Locate every blood parasite and identify its species.
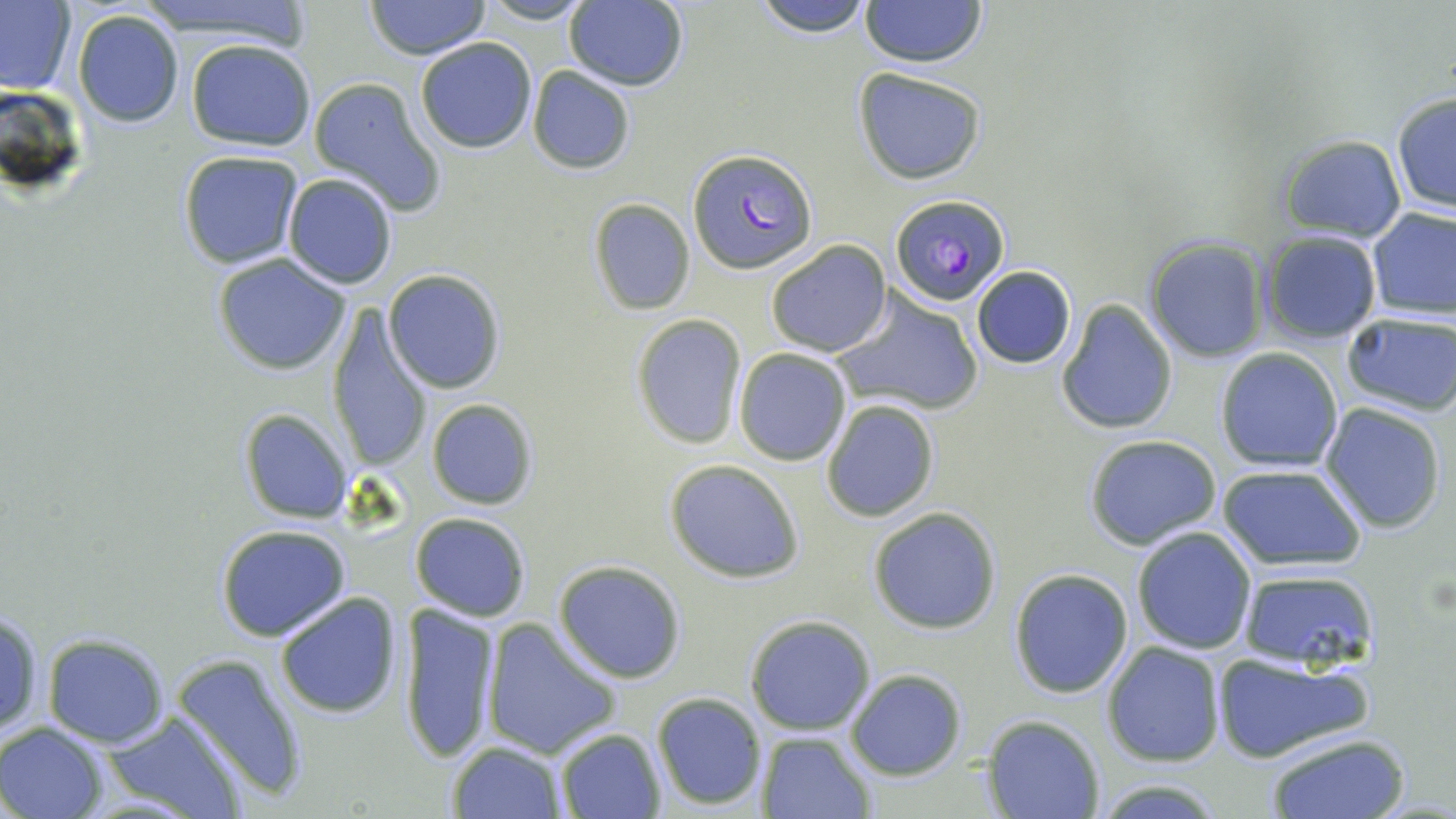
Approximate bounding boxes as (x1, y1, x2, y2) in pixels.
Plasmodium falciparum-infected red blood cells: (688, 148, 814, 274), (890, 194, 1011, 305).
No Plasmodium ovale, Plasmodium malariae, Plasmodium vivax, Babesia divergens, or Trypanosoma brucei observed.

Summary:
  - Uninfected red blood cell locations: (0, 0, 77, 98), (133, 0, 318, 41), (364, 0, 492, 61), (476, 0, 596, 25), (752, 0, 873, 38), (857, 0, 988, 69), (563, 1, 689, 91), (72, 7, 186, 129), (414, 38, 537, 154), (184, 39, 317, 153), (527, 66, 636, 175), (853, 67, 988, 185), (307, 77, 447, 218), (1390, 92, 1455, 214), (1274, 133, 1407, 242), (177, 150, 307, 269), (282, 172, 399, 291), (588, 199, 696, 316), (1366, 208, 1456, 320), (1259, 231, 1382, 346), (1142, 236, 1271, 364), (765, 240, 891, 356), (210, 253, 353, 374), (971, 264, 1076, 368), (383, 269, 507, 394), (831, 291, 985, 417), (1055, 299, 1178, 437), (326, 305, 431, 473), (1340, 313, 1456, 417), (630, 314, 747, 449), (734, 348, 851, 465), (1215, 348, 1344, 471), (425, 397, 540, 511), (821, 400, 940, 520), (1320, 403, 1446, 534), (239, 408, 353, 522), (1083, 435, 1224, 549), (664, 458, 805, 584), (1216, 464, 1368, 571), (868, 508, 1001, 633), (409, 512, 532, 622), (215, 526, 352, 642), (1131, 527, 1257, 654), (553, 560, 688, 683), (1239, 566, 1378, 669), (1008, 568, 1134, 699), (273, 592, 405, 720), (402, 602, 501, 763), (1, 608, 44, 740), (744, 614, 876, 736), (483, 619, 622, 759), (41, 634, 170, 748), (1101, 641, 1226, 766), (172, 653, 309, 804), (1210, 653, 1372, 762), (845, 669, 966, 781), (650, 692, 768, 812), (100, 711, 248, 819), (983, 715, 1103, 819), (0, 720, 109, 819), (553, 728, 666, 818), (756, 731, 875, 817), (1264, 732, 1411, 818), (447, 741, 567, 818), (1088, 777, 1228, 817)
  - Slide-level diagnosis: Plasmodium falciparum
  - Preparation: thin blood film
  - Field of view: single
  - Stain: May-Grünwald-Giemsa
  - Magnification: 1000x
  - Image size: 1456×819 pixels
  - Modality: optical microscopy